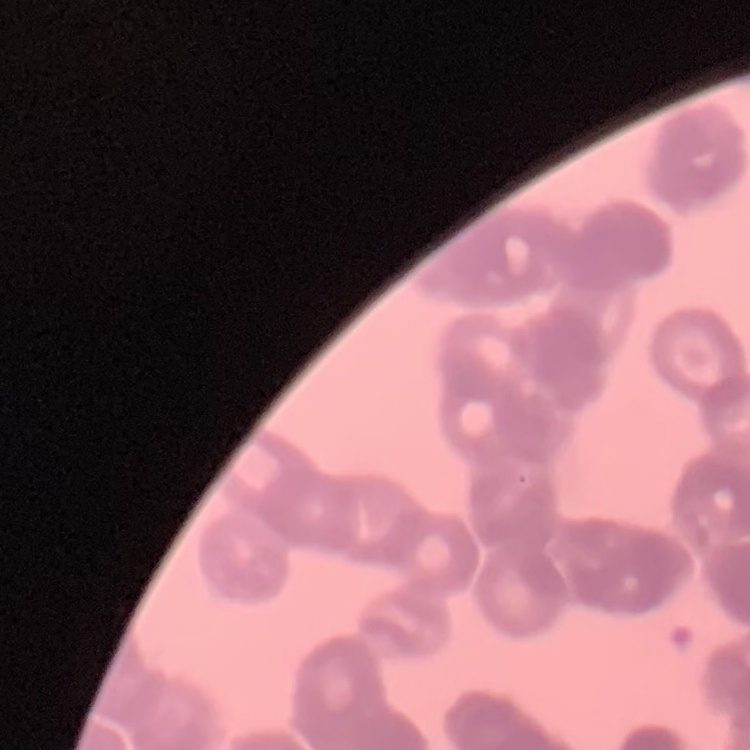

erythrocyte morphology = rouleaux formation
stain = Field's or Giemsa
image type = one tile cut from a larger photomicrograph
preparation = thin blood smear